Classify this cell by malaria status.
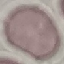

It is uninfected.

Thin blood film. Giemsa-stained preparation. Cell patch, automatically extracted from a larger field of view and resized to 64 × 64 pixels. Photographed with a smartphone camera at the microscope eyepiece.